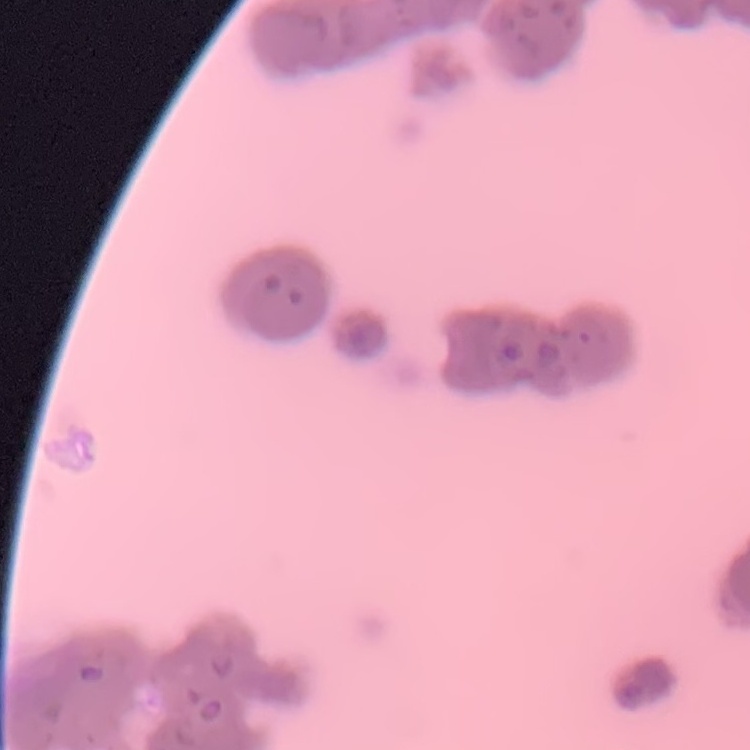

Summary:
  - Red blood cell morphology: rouleaux formation
  - Stain: Field's or Giemsa
  - Image type: one tile cut from a larger photomicrograph
  - Preparation: thin blood film